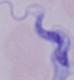 1000x magnification. A trypanosome is seen. Photomicrograph.